Report the malaria status of this cell.
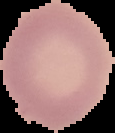

Uninfected.

Cell region segmented out of the field of view; the surrounding area is masked to black. From a thin blood smear. Image is 115×133 pixels.